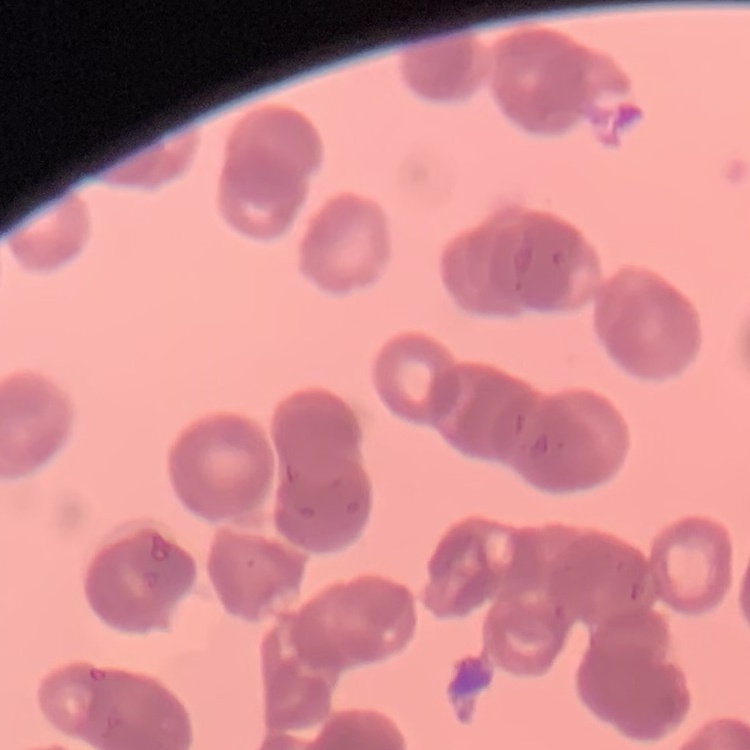

erythrocyte_morphology: rouleaux formation
preparation: thin peripheral smear
stain: Field's or Giemsa
image_type: square crop of a larger photomicrograph